State the preparation type.
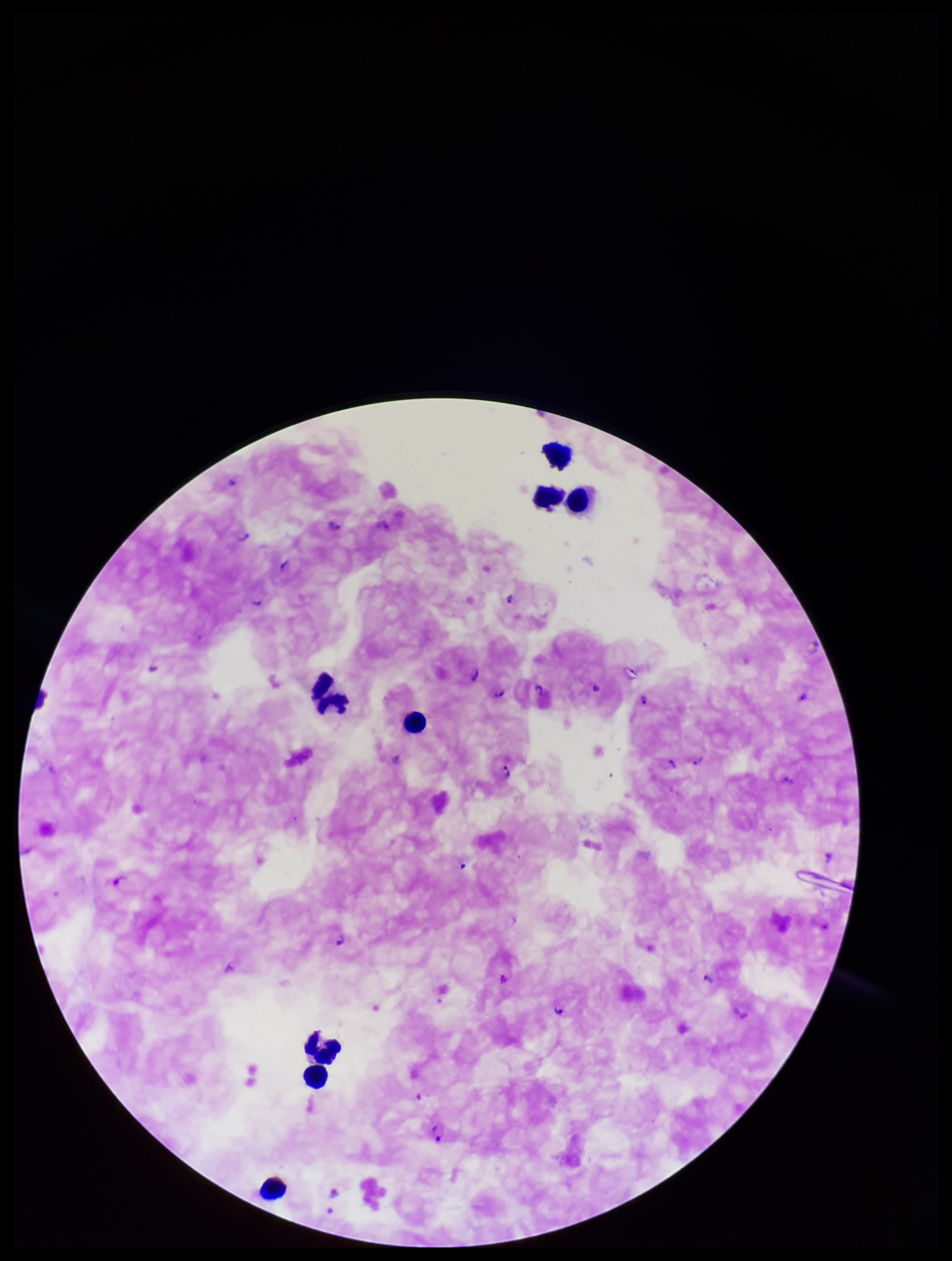
A thick smear.

Summary:
  - Leukocyte count: 24
  - Plasmodium parasites: detected
  - Stain: Giemsa
  - Patient malaria status: infected
  - Parasite count: 8
  - Species reported for this patient: Plasmodium falciparum
  - Image size: 952×1261 pixels
  - Field of view: one from this slide
  - Capture: smartphone photograph through the microscope eyepiece